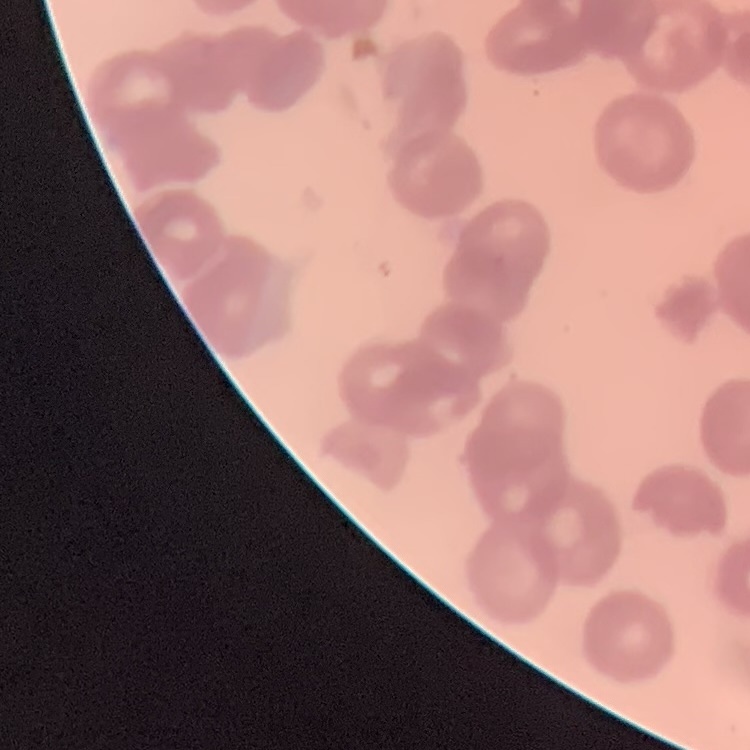 The red blood cells exhibit rouleaux formation. One tile cut from a larger photomicrograph. Thin blood film. Stained with either Field's or Giemsa.